Name the cell type shown.
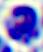

A leukocyte.

400x magnification. Photomicrograph.